Assess this cell for malaria.
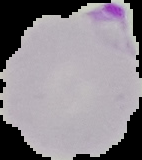

Parasitized.

Image is 142×160 pixels. Segmented cell region on a black background. From a thin blood film.